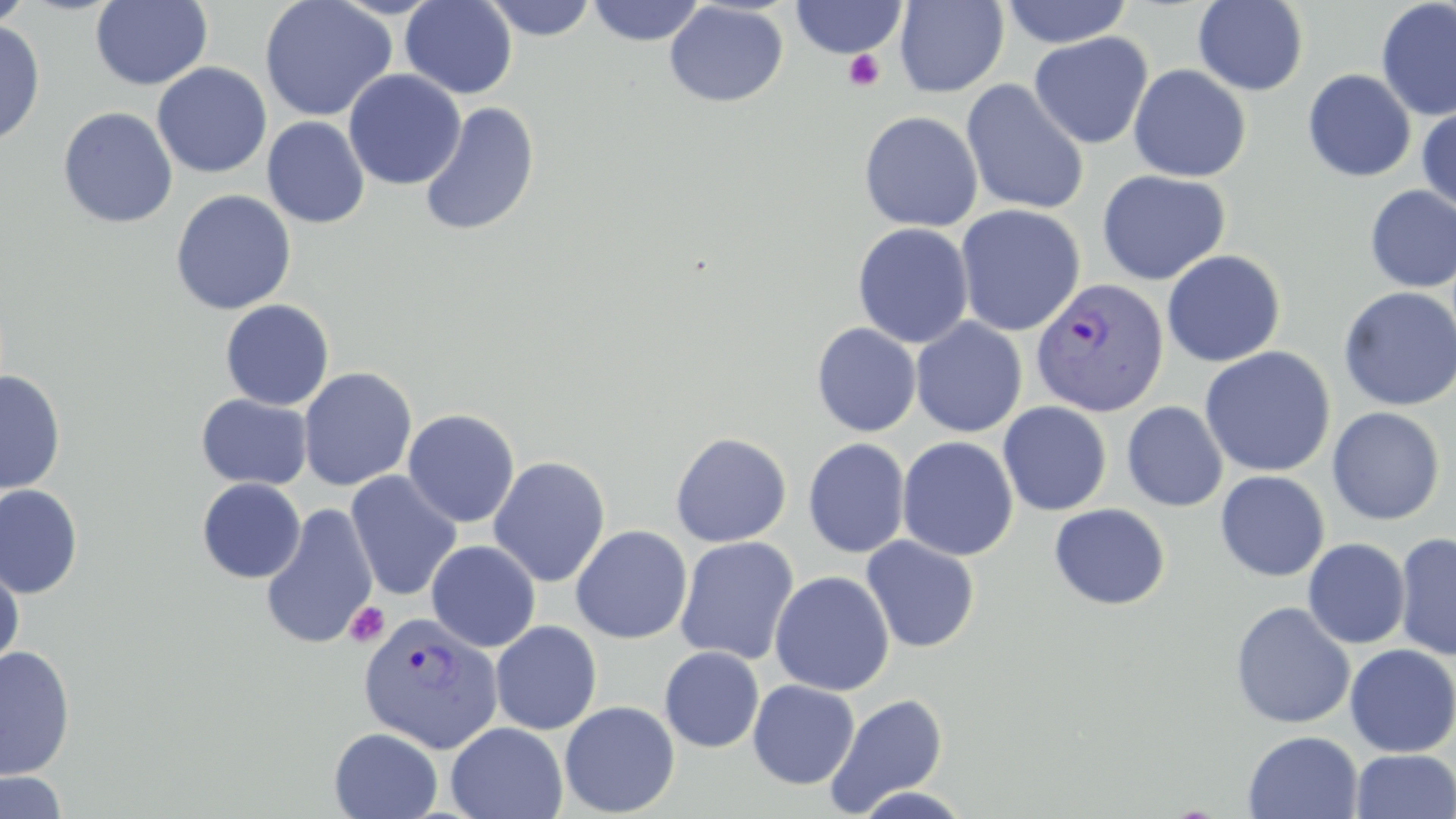
Approximate bounding boxes as (x1, y1, x2, y2) in pixels. Plasmodium vivax-infected red blood cell locations: (1031, 278, 1169, 418), (357, 612, 503, 754). Platelet locations: (842, 50, 886, 92), (344, 602, 390, 648). Uninfected red blood cell locations: (0, 0, 35, 31), (90, 0, 213, 90), (259, 0, 397, 122), (400, 0, 518, 99), (480, 0, 599, 41), (585, 0, 708, 47), (790, 0, 908, 59), (893, 0, 1009, 97), (1000, 0, 1134, 49), (1193, 0, 1309, 96), (1376, 0, 1456, 122), (664, 2, 789, 108), (0, 18, 45, 148), (1029, 32, 1153, 150), (152, 62, 272, 178), (1128, 65, 1251, 182), (343, 69, 466, 190), (1302, 69, 1417, 182), (960, 79, 1090, 216), (418, 102, 540, 237), (1416, 105, 1456, 215), (58, 107, 178, 229), (858, 111, 982, 232), (262, 116, 370, 229), (1097, 170, 1231, 286), (1364, 186, 1456, 293), (171, 189, 296, 315), (955, 204, 1085, 336), (852, 222, 974, 349), (1161, 249, 1285, 367), (1338, 286, 1456, 411), (220, 300, 334, 411), (910, 318, 1027, 438), (811, 322, 922, 437), (1199, 346, 1337, 478), (298, 367, 417, 491), (0, 370, 66, 494), (195, 394, 312, 490), (998, 401, 1112, 516), (1122, 401, 1228, 512), (1327, 406, 1445, 525), (403, 408, 520, 528), (670, 432, 792, 547), (897, 436, 1019, 561), (803, 438, 911, 558), (488, 455, 611, 588), (1214, 470, 1330, 581), (345, 471, 462, 602), (196, 478, 306, 584), (0, 484, 83, 599), (260, 503, 378, 650), (1049, 503, 1170, 610), (570, 525, 693, 644), (1394, 531, 1456, 661), (674, 536, 800, 666), (861, 536, 980, 653), (1303, 538, 1410, 649), (426, 540, 541, 652), (0, 558, 25, 674), (770, 570, 895, 696), (1230, 600, 1356, 729), (489, 620, 602, 735), (1344, 643, 1456, 758), (0, 646, 76, 781), (659, 646, 764, 752), (748, 679, 860, 789), (824, 693, 949, 816), (559, 700, 680, 817), (446, 722, 568, 819), (329, 728, 443, 818), (1242, 731, 1363, 818), (1350, 750, 1456, 819), (0, 770, 68, 818). Slide-level diagnosis: Plasmodium vivax. Thin blood film. Light microscopy. 1000x magnification. May-Grünwald-Giemsa stain. One field of a larger specimen. Image is 1456×819 pixels.